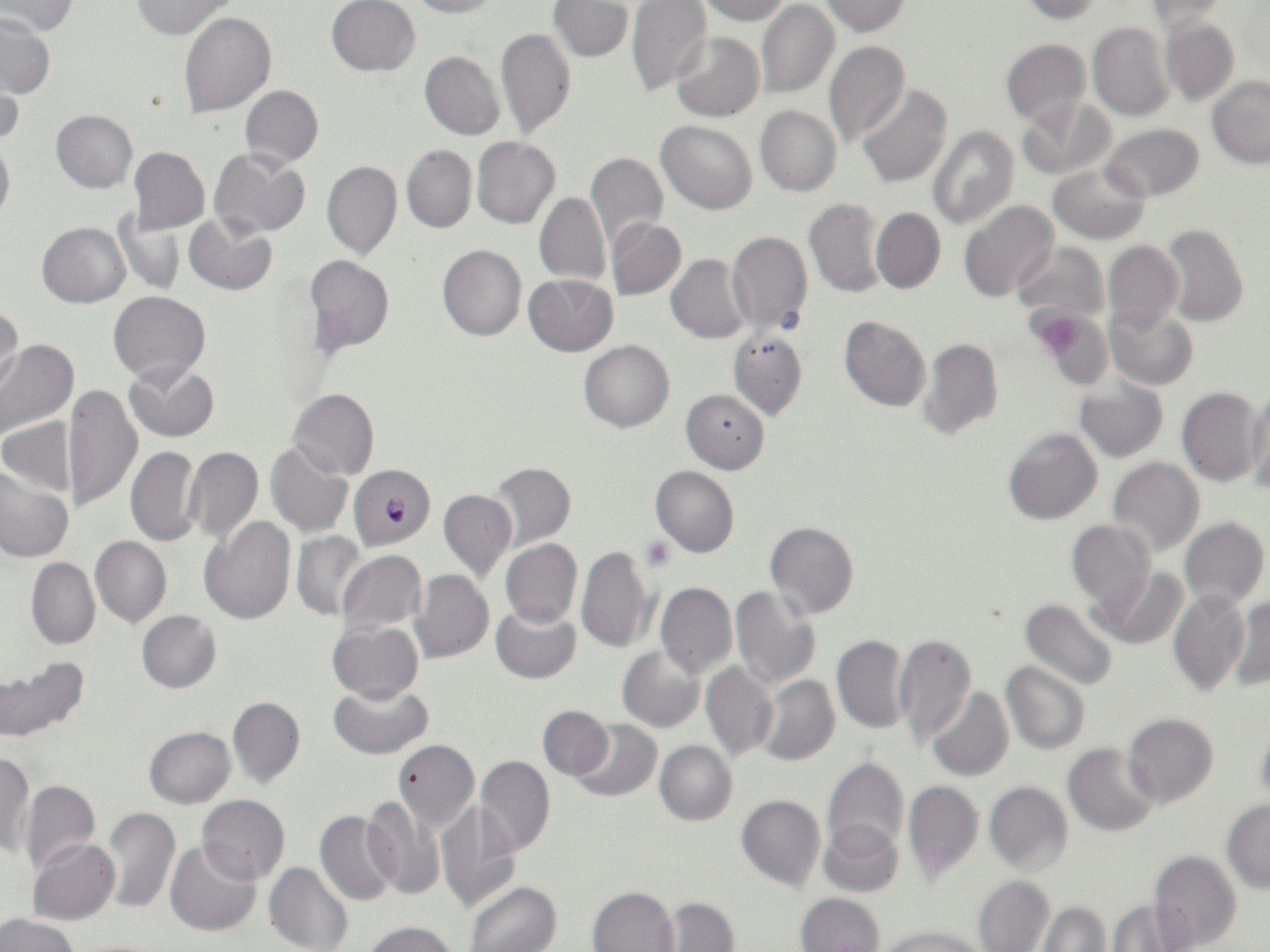
{
  "slide_level_diagnosis": "Plasmodium falciparum",
  "modality": "light microscopy",
  "image_size": "1270×952 pixels",
  "field_of_view": "one of a larger specimen",
  "preparation": "thin blood film",
  "platelet_locations": "approximate bounding boxes as (x1, y1, x2, y2) in pixels: (1038, 318, 1087, 361), (642, 537, 675, 570)",
  "stain": "May-Grünwald-Giemsa",
  "magnification": "1000x",
  "plasmodium_falciparum_infected_red_blood_cell_locations": "approximate bounding boxes as (x1, y1, x2, y2) in pixels: (349, 465, 435, 550)",
  "uninfected_red_blood_cell_locations": "approximate bounding boxes as (x1, y1, x2, y2) in pixels: (326, 0, 421, 76), (405, 0, 500, 18), (694, 0, 790, 23), (1016, 0, 1104, 23), (3, 1, 78, 36), (132, 1, 237, 40), (550, 1, 634, 61), (628, 1, 712, 96), (818, 1, 911, 36), (757, 2, 839, 100), (1141, 3, 1227, 30), (0, 12, 53, 99), (180, 12, 275, 117), (1159, 15, 1240, 107), (1088, 22, 1174, 120), (495, 26, 576, 140), (670, 31, 764, 122), (1002, 39, 1090, 126), (824, 40, 909, 146), (420, 51, 504, 139), (1, 71, 22, 149), (1207, 76, 1270, 166), (856, 85, 952, 188), (241, 86, 322, 168), (1019, 96, 1113, 178), (755, 105, 841, 196), (51, 109, 138, 192), (657, 119, 756, 213), (1101, 123, 1205, 201), (928, 126, 1018, 230), (0, 134, 14, 225), (472, 136, 559, 228), (402, 145, 476, 232), (129, 147, 209, 234), (209, 148, 311, 238), (585, 152, 668, 248), (322, 159, 401, 260), (1047, 161, 1150, 245), (535, 192, 610, 287), (805, 198, 888, 298), (960, 201, 1058, 302), (871, 208, 945, 293), (115, 212, 186, 297), (185, 214, 276, 295), (607, 218, 686, 300), (38, 222, 130, 308), (1161, 223, 1247, 326), (727, 232, 813, 338), (1103, 241, 1183, 335), (437, 243, 526, 341), (1013, 243, 1108, 324), (304, 255, 393, 355), (667, 255, 750, 343), (524, 274, 618, 355), (109, 291, 209, 384), (1, 301, 22, 393), (1106, 306, 1197, 390), (1027, 307, 1112, 383), (840, 315, 930, 411), (728, 329, 807, 420), (0, 338, 78, 441), (919, 338, 1002, 439), (580, 340, 674, 432), (124, 362, 217, 441), (1075, 380, 1168, 462), (64, 384, 142, 514), (289, 387, 379, 479), (1177, 388, 1264, 487), (681, 389, 769, 473), (1246, 389, 1270, 496), (2, 418, 77, 496), (1004, 427, 1102, 525), (265, 441, 353, 538), (185, 446, 262, 545), (126, 447, 201, 546), (1107, 458, 1203, 556), (489, 462, 575, 549), (0, 465, 72, 562), (650, 465, 738, 557), (439, 490, 515, 582), (199, 516, 296, 623), (1180, 518, 1269, 612), (765, 521, 859, 618), (1067, 521, 1155, 611), (292, 532, 366, 619), (91, 535, 170, 627), (501, 539, 582, 627), (576, 545, 652, 653), (336, 550, 426, 633), (27, 558, 99, 646), (1096, 566, 1189, 651), (409, 569, 494, 663), (656, 583, 735, 679), (730, 585, 819, 690), (1169, 587, 1250, 698), (1230, 595, 1269, 693), (1021, 599, 1118, 692), (490, 603, 580, 681), (137, 610, 220, 693), (329, 621, 423, 702), (893, 633, 975, 749), (831, 634, 908, 733), (618, 645, 704, 732), (0, 658, 89, 742), (700, 661, 778, 760), (1001, 662, 1089, 754), (755, 674, 840, 766), (329, 682, 431, 758), (926, 686, 1013, 782), (228, 696, 305, 788), (538, 705, 613, 778), (1124, 713, 1218, 807), (1255, 716, 1270, 807), (572, 719, 660, 801), (144, 726, 235, 808), (393, 739, 478, 831), (656, 740, 736, 824), (1064, 743, 1159, 836), (2, 752, 33, 858), (477, 755, 554, 858), (822, 757, 908, 860), (450, 769, 545, 896), (19, 780, 100, 877), (902, 781, 983, 882), (985, 782, 1072, 875), (361, 794, 445, 898), (736, 794, 825, 891), (198, 795, 290, 884), (1222, 800, 1270, 893), (437, 805, 521, 913), (102, 807, 180, 913), (316, 812, 400, 906), (819, 819, 903, 898), (28, 840, 120, 924), (165, 840, 260, 935), (1150, 850, 1241, 952), (264, 863, 353, 952), (973, 875, 1054, 952), (467, 881, 562, 952), (588, 886, 678, 951), (797, 892, 884, 952), (661, 897, 737, 951), (1106, 899, 1191, 951), (1038, 901, 1110, 951), (0, 913, 80, 952), (365, 921, 459, 952), (878, 925, 987, 952)"
}